Classify this cell by malaria status.
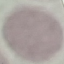

It is uninfected.

Automatically extracted cell patch, resized to 64 × 64 pixels. Giemsa stain. Thin blood smear. Acquired by smartphone through the microscope eyepiece.